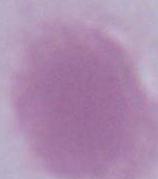
Summary:
  - Modality: micrograph
  - Magnification: 1000x
  - Identification: red blood cell